Locate every blood parasite and identify its species.
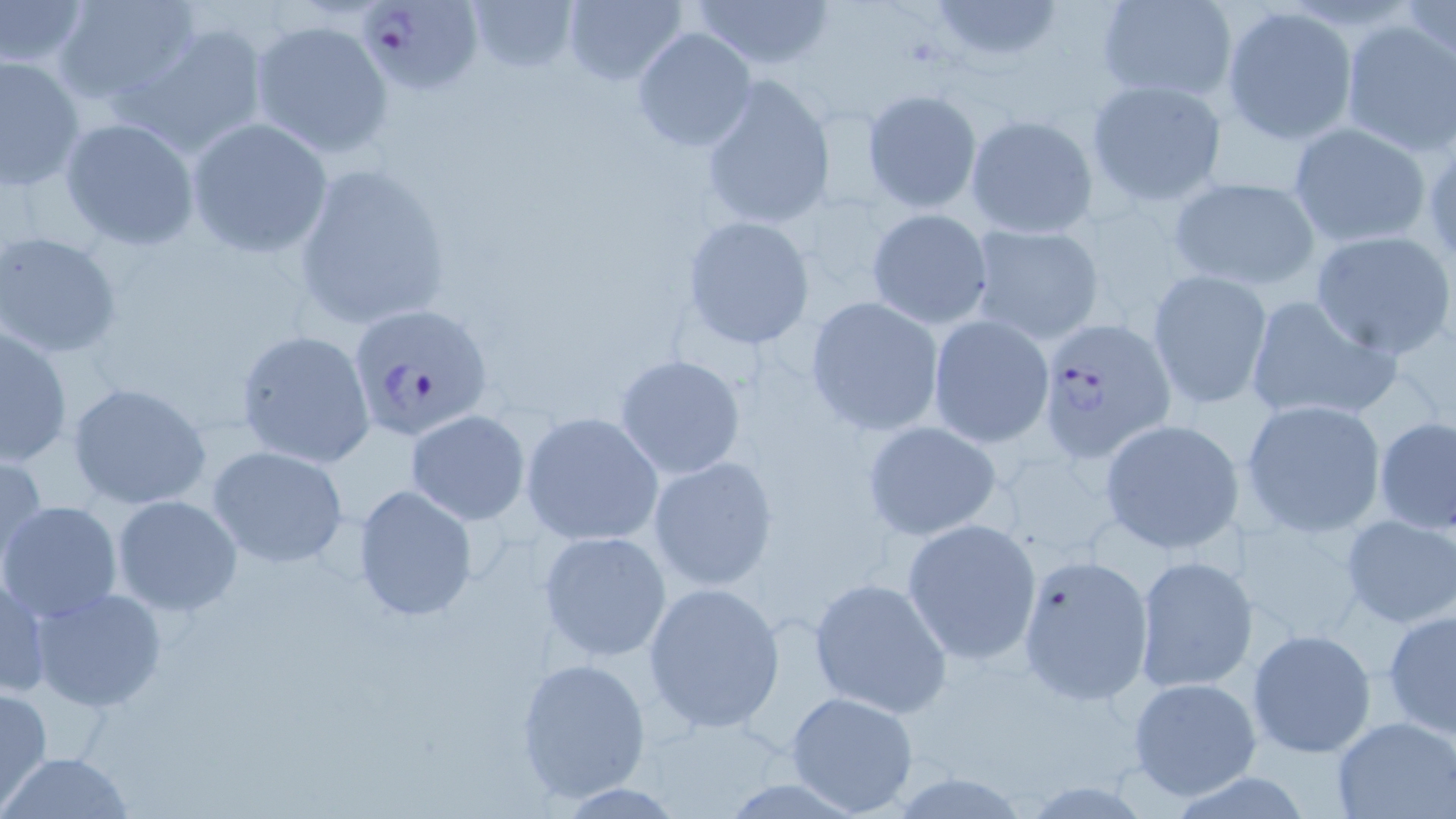

Approximate bounding boxes as (x1,y1)-(x2,y2) corner pairs in pixels.
Plasmodium falciparum-infected red blood cells: (361,0)-(485,95), (348,303)-(494,442), (1035,317)-(1177,463).
No Plasmodium ovale, Plasmodium malariae, Plasmodium vivax, Babesia divergens, or Trypanosoma brucei observed.

slide-level diagnosis = Plasmodium falciparum
stain = May-Grünwald-Giemsa
preparation = thin blood film
field of view = single
modality = optical microscopy
image size = 1456×819 pixels
magnification = 1000x
uninfected red blood cell locations = approximate bounding boxes as (x1,y1)-(x2,y2) corner pairs in pixels: (0,0)-(89,73), (53,0)-(202,109), (468,0)-(578,77), (690,0)-(836,71), (929,0)-(1063,67), (1094,0)-(1240,104), (561,1)-(688,85), (1221,6)-(1360,144), (1337,17)-(1455,155), (250,18)-(393,157), (122,20)-(270,162), (632,27)-(758,153), (0,54)-(85,191), (698,77)-(835,232), (1085,78)-(1227,208), (861,89)-(982,214), (964,114)-(1098,239), (60,117)-(200,250), (186,118)-(334,258), (1287,122)-(1434,248), (292,161)-(452,330), (1165,176)-(1320,292), (866,207)-(993,328), (681,215)-(815,351), (965,223)-(1105,346), (1307,228)-(1456,360), (0,231)-(122,360), (1146,271)-(1274,408), (1243,294)-(1401,427), (805,296)-(948,436), (928,315)-(1054,447), (2,324)-(73,465), (236,329)-(377,469), (614,353)-(747,481), (66,381)-(212,510), (1241,399)-(1387,537), (405,409)-(530,526), (520,412)-(664,546), (1374,415)-(1456,535), (1098,417)-(1247,556), (862,421)-(1004,541), (207,446)-(350,568), (0,451)-(48,571), (647,455)-(779,592), (352,483)-(480,622), (111,494)-(242,618), (1,502)-(123,624), (1227,511)-(1374,648), (1340,513)-(1456,630), (901,518)-(1043,666), (538,529)-(671,662), (1015,553)-(1154,707), (1134,555)-(1258,694), (0,563)-(50,702), (808,576)-(952,717), (644,582)-(786,733), (29,587)-(167,713), (1382,607)-(1456,739), (1247,628)-(1378,760), (514,656)-(654,804), (1126,675)-(1262,803), (0,687)-(53,809), (785,691)-(920,816), (1332,715)-(1454,819), (2,750)-(135,819)